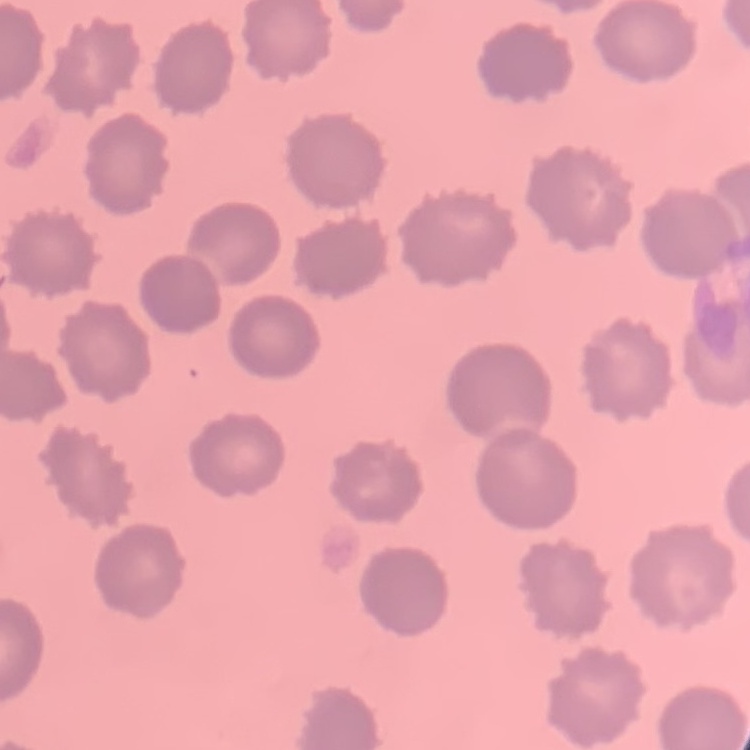

Summary:
  - Red blood cell morphology: no rouleaux formation
  - Stain: Field's or Giemsa
  - Preparation: thin blood film
  - Image type: one tile cut from a larger photomicrograph